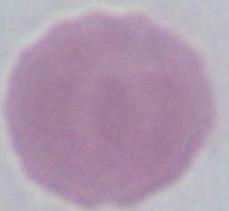

Summary:
  - Magnification: 1000x
  - Modality: micrograph
  - Identification: red blood cell